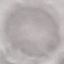

Summary:
  - Result: no malaria parasites detected
  - Capture: smartphone camera at the microscope eyepiece
  - Stain: Giemsa
  - Preparation: thin smear
  - Image type: automatically extracted cell patch, resized to 64 × 64 pixels